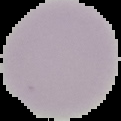
Summary:
  - Image type: cell region segmented out of the field of view; surrounding area masked to black
  - Image size: 121×121 pixels
  - Preparation: thin blood smear
  - Result: no Plasmodium parasites seen